Classify this cell by malaria status.
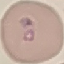

It is parasitized.

Automatically extracted cell patch, resized to 64 × 64 pixels. Giemsa stain. Acquired by smartphone through the microscope eyepiece. Thin blood smear.